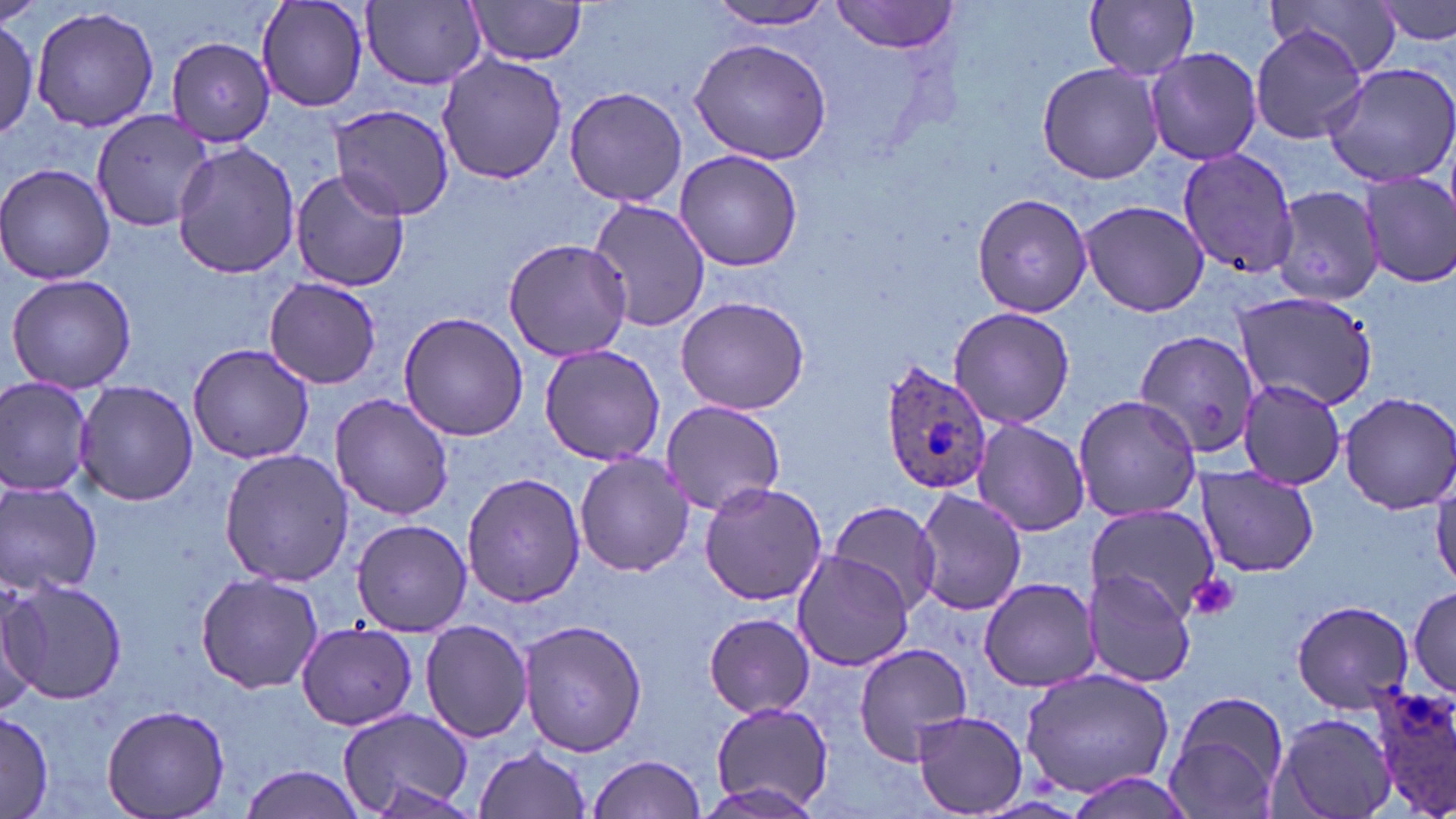
Approximate bounding boxes as named x1/y1/x2/y2 corners in pixels. Platelet locations: (x1=1187, y1=572, x2=1240, y2=621). Plasmodium ovale-infected red blood cell locations: (x1=878, y1=362, x2=996, y2=499), (x1=1371, y1=681, x2=1455, y2=819). Uninfected red blood cell locations: (x1=256, y1=0, x2=369, y2=111), (x1=710, y1=0, x2=839, y2=30), (x1=1085, y1=0, x2=1201, y2=80), (x1=1270, y1=0, x2=1405, y2=80), (x1=1375, y1=0, x2=1456, y2=51), (x1=363, y1=1, x2=487, y2=89), (x1=464, y1=1, x2=590, y2=66), (x1=832, y1=1, x2=956, y2=53), (x1=31, y1=5, x2=160, y2=135), (x1=0, y1=16, x2=39, y2=139), (x1=1248, y1=26, x2=1368, y2=146), (x1=168, y1=36, x2=277, y2=146), (x1=688, y1=36, x2=833, y2=167), (x1=1144, y1=46, x2=1262, y2=166), (x1=437, y1=53, x2=568, y2=186), (x1=1321, y1=61, x2=1456, y2=188), (x1=1036, y1=62, x2=1165, y2=186), (x1=564, y1=86, x2=689, y2=208), (x1=333, y1=105, x2=456, y2=219), (x1=90, y1=108, x2=216, y2=233), (x1=173, y1=141, x2=300, y2=280), (x1=1176, y1=145, x2=1301, y2=282), (x1=672, y1=150, x2=804, y2=272), (x1=0, y1=162, x2=116, y2=285), (x1=290, y1=170, x2=410, y2=291), (x1=1359, y1=172, x2=1456, y2=290), (x1=1273, y1=185, x2=1387, y2=305), (x1=970, y1=190, x2=1094, y2=320), (x1=588, y1=197, x2=710, y2=334), (x1=1079, y1=199, x2=1209, y2=316), (x1=502, y1=240, x2=633, y2=361), (x1=4, y1=272, x2=136, y2=393), (x1=264, y1=276, x2=382, y2=387), (x1=1230, y1=290, x2=1379, y2=411), (x1=674, y1=295, x2=810, y2=416), (x1=947, y1=306, x2=1076, y2=431), (x1=398, y1=314, x2=531, y2=442), (x1=1128, y1=326, x2=1260, y2=468), (x1=187, y1=341, x2=314, y2=463), (x1=538, y1=343, x2=670, y2=465), (x1=0, y1=379, x2=94, y2=497), (x1=1236, y1=379, x2=1348, y2=489), (x1=74, y1=380, x2=198, y2=505), (x1=331, y1=391, x2=455, y2=521), (x1=1336, y1=391, x2=1456, y2=514), (x1=1071, y1=394, x2=1204, y2=522), (x1=660, y1=400, x2=785, y2=517), (x1=971, y1=420, x2=1091, y2=535), (x1=218, y1=448, x2=352, y2=589), (x1=573, y1=452, x2=696, y2=577), (x1=1194, y1=468, x2=1319, y2=577), (x1=461, y1=472, x2=587, y2=609), (x1=0, y1=479, x2=103, y2=598), (x1=698, y1=481, x2=830, y2=607), (x1=912, y1=488, x2=1027, y2=615), (x1=827, y1=499, x2=944, y2=614), (x1=1087, y1=505, x2=1217, y2=618), (x1=352, y1=520, x2=473, y2=636), (x1=791, y1=552, x2=916, y2=672), (x1=1082, y1=569, x2=1195, y2=687), (x1=195, y1=572, x2=325, y2=696), (x1=4, y1=574, x2=127, y2=706), (x1=977, y1=577, x2=1104, y2=692), (x1=1411, y1=585, x2=1455, y2=699), (x1=0, y1=589, x2=46, y2=715), (x1=1288, y1=599, x2=1416, y2=714), (x1=703, y1=612, x2=815, y2=717), (x1=518, y1=618, x2=649, y2=757), (x1=420, y1=619, x2=534, y2=744), (x1=297, y1=622, x2=417, y2=731), (x1=852, y1=641, x2=975, y2=766), (x1=1020, y1=669, x2=1176, y2=797), (x1=1163, y1=691, x2=1290, y2=815), (x1=101, y1=701, x2=231, y2=819), (x1=708, y1=701, x2=836, y2=813), (x1=337, y1=707, x2=473, y2=817), (x1=911, y1=708, x2=1028, y2=815), (x1=1271, y1=709, x2=1396, y2=819), (x1=0, y1=712, x2=56, y2=817), (x1=472, y1=745, x2=593, y2=819), (x1=586, y1=753, x2=707, y2=819), (x1=240, y1=764, x2=367, y2=818), (x1=1063, y1=769, x2=1198, y2=818), (x1=361, y1=776, x2=475, y2=817). Slide-level diagnosis: Plasmodium ovale. May-Grünwald-Giemsa-stained preparation. Thin blood film. Optical microscopy. Image is 1456×819 pixels. 1000x magnification. One field of a larger specimen.